Locate every blood parasite and identify its species.
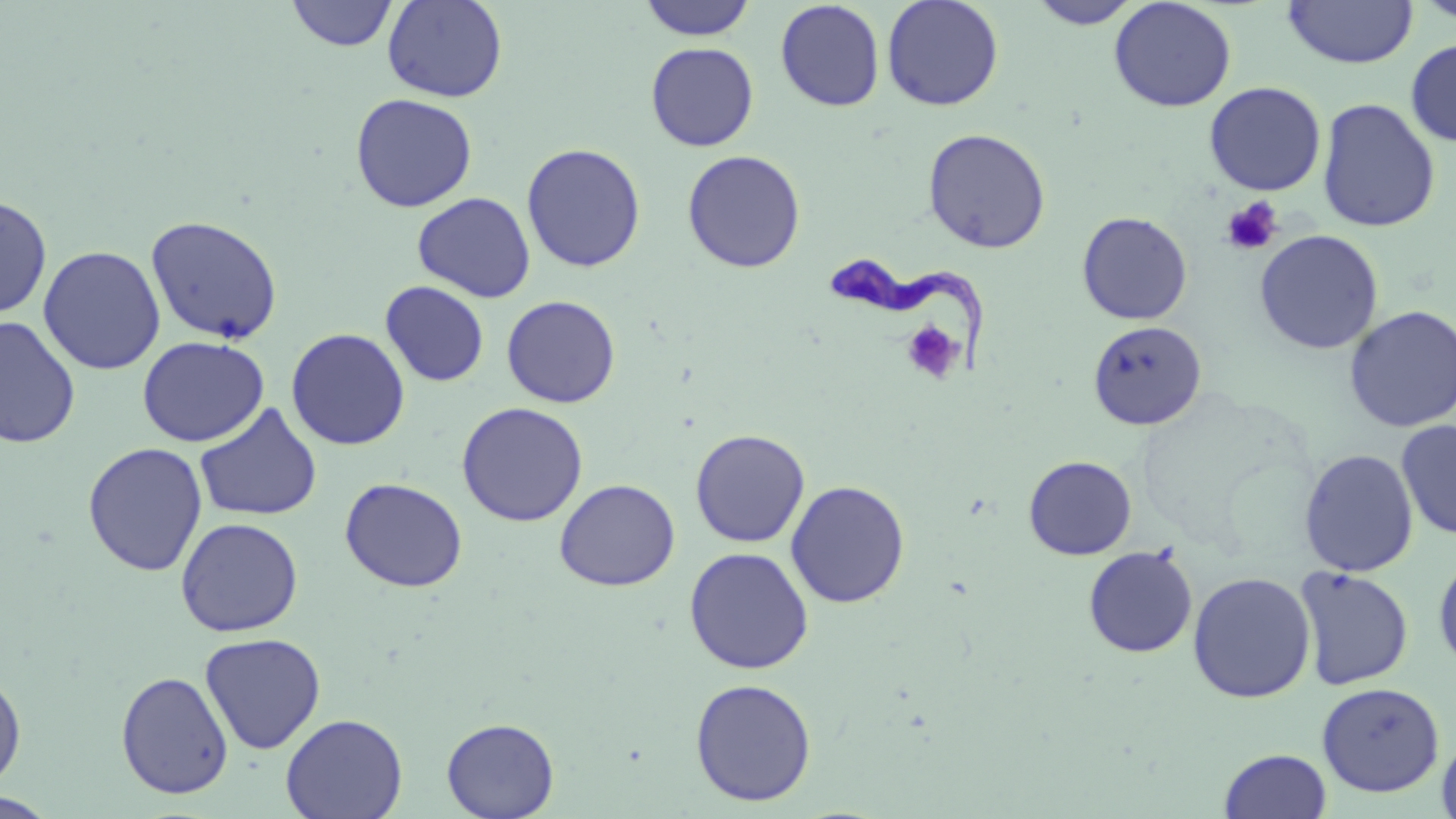
Approximate bounding boxes as (x1,y1)-(x2,y2) corner pairs in pixels.
Trypanosoma brucei: (822,258)-(988,376).
No Plasmodium falciparum, Plasmodium ovale, Plasmodium malariae, Plasmodium vivax, or Babesia divergens observed.

slide-level diagnosis = Trypanosoma brucei
image size = 1456×819 pixels
modality = optical microscopy
platelet locations = approximate bounding boxes as (x1,y1)-(x2,y2) corner pairs in pixels: (1221,197)-(1284,256), (901,321)-(964,385)
uninfected red blood cell locations = approximate bounding boxes as (x1,y1)-(x2,y2) corner pairs in pixels: (382,0)-(508,103), (638,0)-(757,41), (881,0)-(1004,111), (1108,0)-(1237,112), (1283,0)-(1417,68), (1413,0)-(1456,26), (285,1)-(399,51), (775,1)-(885,112), (1027,1)-(1142,29), (1405,38)-(1456,146), (646,42)-(759,151), (1203,81)-(1326,196), (349,93)-(478,212), (1317,98)-(1440,233), (922,128)-(1051,254), (522,143)-(646,273), (682,149)-(806,274), (413,191)-(535,303), (0,195)-(52,319), (1076,211)-(1193,325), (145,214)-(283,345), (1254,229)-(1384,355), (38,245)-(165,375), (380,280)-(489,387), (501,295)-(621,408), (1344,305)-(1456,433), (0,315)-(80,449), (1088,321)-(1207,431), (286,328)-(410,451), (137,335)-(268,447), (456,401)-(588,527), (195,402)-(322,522), (1396,419)-(1456,541), (690,428)-(810,548), (82,442)-(208,576), (1299,449)-(1418,577), (1023,455)-(1137,560), (339,477)-(468,593), (555,478)-(680,591), (785,480)-(910,608), (175,517)-(303,636), (1083,545)-(1198,658), (684,547)-(814,674), (1433,551)-(1456,673), (1294,566)-(1414,690), (1187,571)-(1316,703), (199,632)-(326,754), (0,671)-(26,791), (116,671)-(234,799), (689,678)-(817,806), (1317,681)-(1444,797), (280,713)-(407,819), (441,717)-(559,819), (1437,733)-(1456,819), (1219,748)-(1331,819), (0,793)-(59,818)
preparation = thin blood smear
magnification = 1000x
stain = May-Grünwald-Giemsa
field of view = single